State which parasite is depicted.
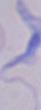
This is a trypanosome.

Summary:
  - Magnification: 1000x
  - Modality: photomicrograph